Report the malaria status of this cell.
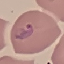
It is parasitized.

stain = Giemsa
image type = automatically extracted cell patch, resized to 64 × 64 pixels
preparation = thin blood film
capture = smartphone camera at the microscope eyepiece